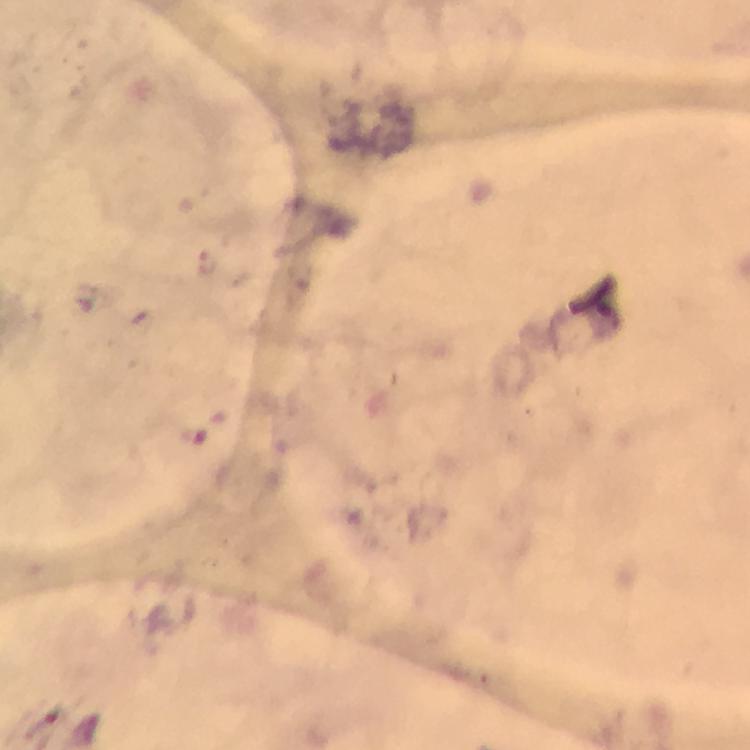
Approximate object centers, in pixels from the top-left corner.
Summary:
  - Plasmodium parasite locations: (x=208, y=264)
  - Stain: Giemsa
  - Image size: 750×750 pixels
  - Capture: smartphone mounted on the microscope
  - Preparation: thick smear
  - Magnification: 100x
  - Context: from a diagnostic examination for malaria
  - Cropped from: a single field of view
  - Immersion oil: used